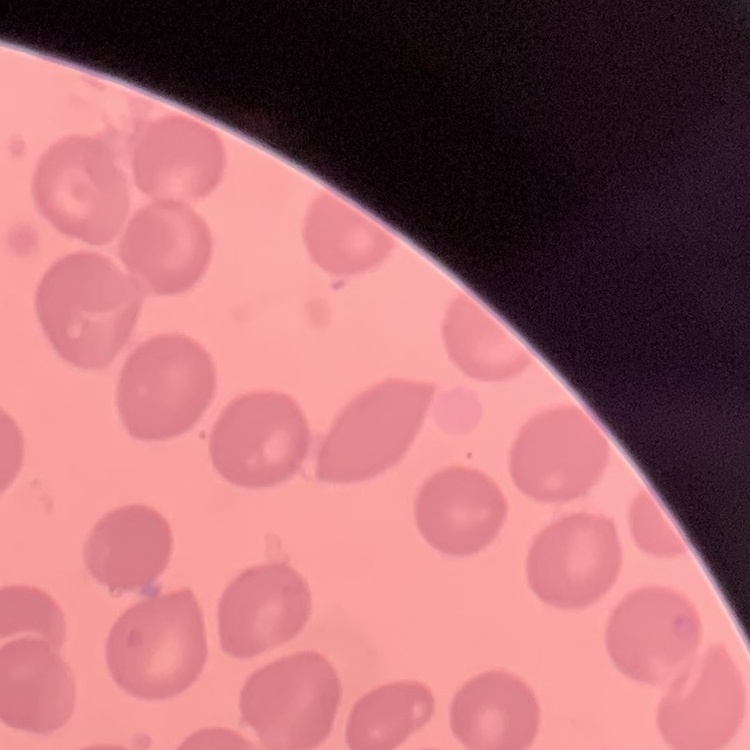

red blood cell morphology = no rouleaux formation
preparation = thin blood film
image type = square crop of a larger photomicrograph
stain = Field's or Giemsa